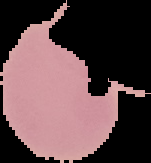 From a thin blood film. The area outside the segmented cell region is set to black. Malaria status: uninfected. Image is 151×163 pixels.